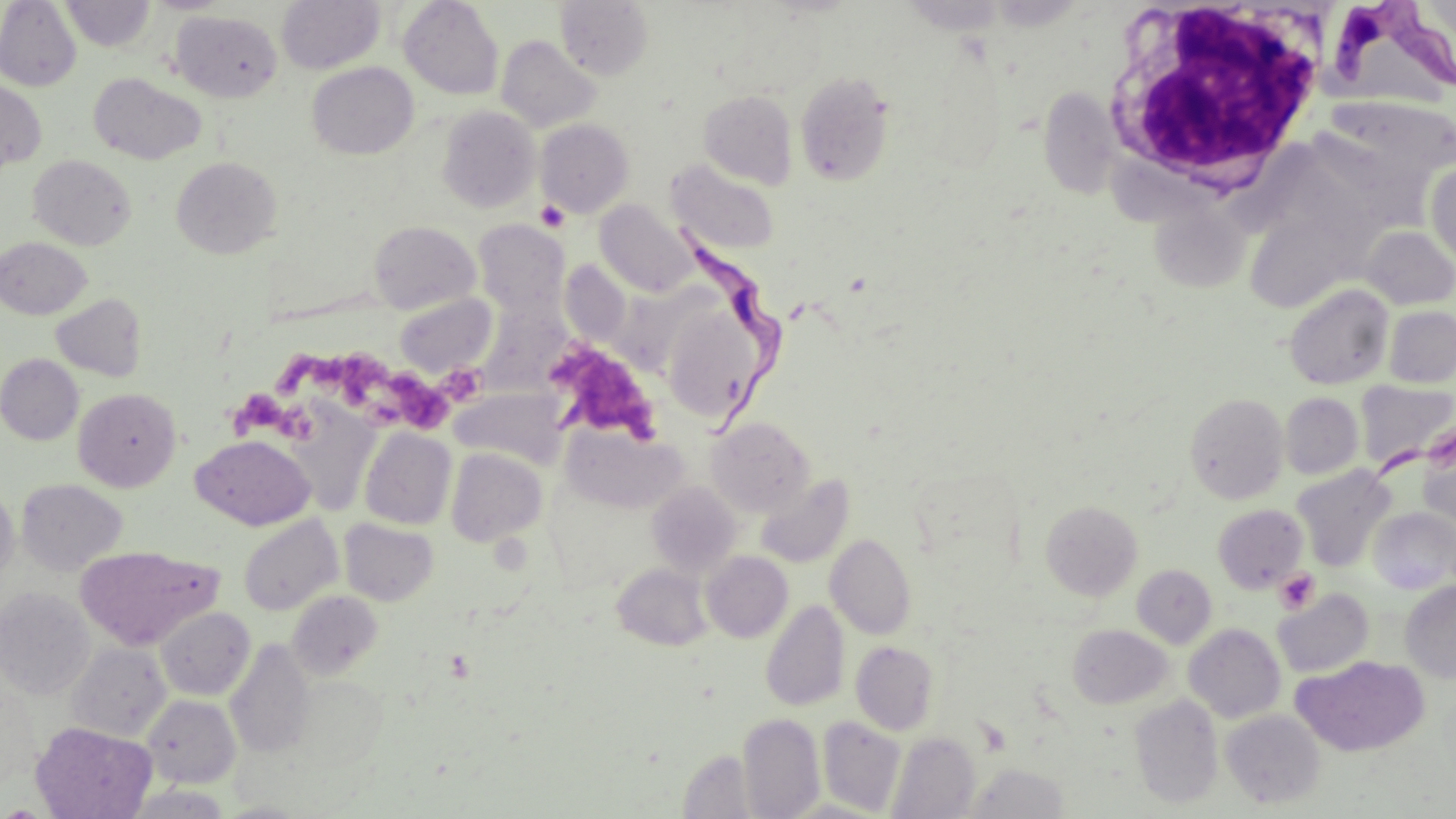

Summary:
  - Coordinate format: approximate bounding boxes as (x1,y1)-(x2,y2) corner pairs in pixels
  - Uninfected red blood cell locations: (59,0)-(156,52), (144,0)-(234,14), (276,0)-(385,74), (398,0)-(504,101), (555,0)-(653,80), (900,0)-(1010,34), (0,1)-(82,91), (170,10)-(282,102), (496,35)-(601,133), (307,62)-(419,160), (795,71)-(895,187), (88,73)-(206,165), (0,81)-(46,170), (1039,86)-(1121,198), (699,89)-(798,189), (1320,96)-(1456,202), (437,106)-(540,213), (535,118)-(634,217), (28,154)-(136,250), (171,156)-(281,259), (666,160)-(780,256), (1426,161)-(1456,266), (1148,199)-(1252,295), (594,200)-(698,297), (1244,203)-(1368,313), (473,220)-(569,315), (368,221)-(480,313), (1360,226)-(1456,309), (1,237)-(91,319), (1285,284)-(1393,390), (51,293)-(147,381), (395,294)-(497,378), (663,305)-(770,425), (1384,306)-(1456,388), (0,354)-(84,445), (1355,380)-(1456,472), (450,387)-(567,467), (73,388)-(181,492), (1185,392)-(1289,504), (1280,393)-(1363,479), (286,404)-(381,515), (706,417)-(814,516), (1418,424)-(1456,529), (564,426)-(687,514), (359,428)-(456,530), (191,434)-(316,530), (446,448)-(547,547), (1292,465)-(1395,572), (756,473)-(854,568), (16,479)-(127,576), (646,481)-(742,578), (0,486)-(19,587), (1040,500)-(1143,601), (1213,504)-(1308,593), (1369,508)-(1456,595), (238,515)-(343,616), (338,519)-(438,606), (825,533)-(916,639), (75,544)-(221,651), (701,551)-(793,642), (612,563)-(712,651), (1132,564)-(1217,648), (1400,581)-(1456,683), (0,588)-(95,699), (287,589)-(383,680), (1273,589)-(1374,678), (761,600)-(850,712), (156,606)-(255,700), (1068,624)-(1173,709), (1184,624)-(1286,723), (225,638)-(315,758), (851,641)-(939,735), (65,642)-(171,742), (1291,655)-(1430,757), (289,675)-(387,769), (0,682)-(42,789), (1129,694)-(1223,809), (142,695)-(241,787), (1221,710)-(1325,809), (737,713)-(825,818), (818,716)-(906,815), (30,722)-(157,819), (887,731)-(980,819), (961,762)-(1072,819), (123,786)-(233,819)
  - Trypanosoma brucei locations: (1335,5)-(1455,90), (673,215)-(804,443)
  - Platelet locations: (535,199)-(569,232), (544,337)-(661,443), (275,348)-(395,406), (387,371)-(450,431), (228,387)-(293,443), (1274,569)-(1319,614)
  - White blood cell locations: (1097,5)-(1332,202)
  - Slide-level diagnosis: Trypanosoma brucei
  - Image size: 1456×819 pixels
  - Field of view: single
  - Stain: May-Grünwald-Giemsa
  - Modality: optical microscopy
  - Preparation: thin blood film
  - Magnification: 1000x